Point out each malaria parasite and classify it by life-cycle stage.
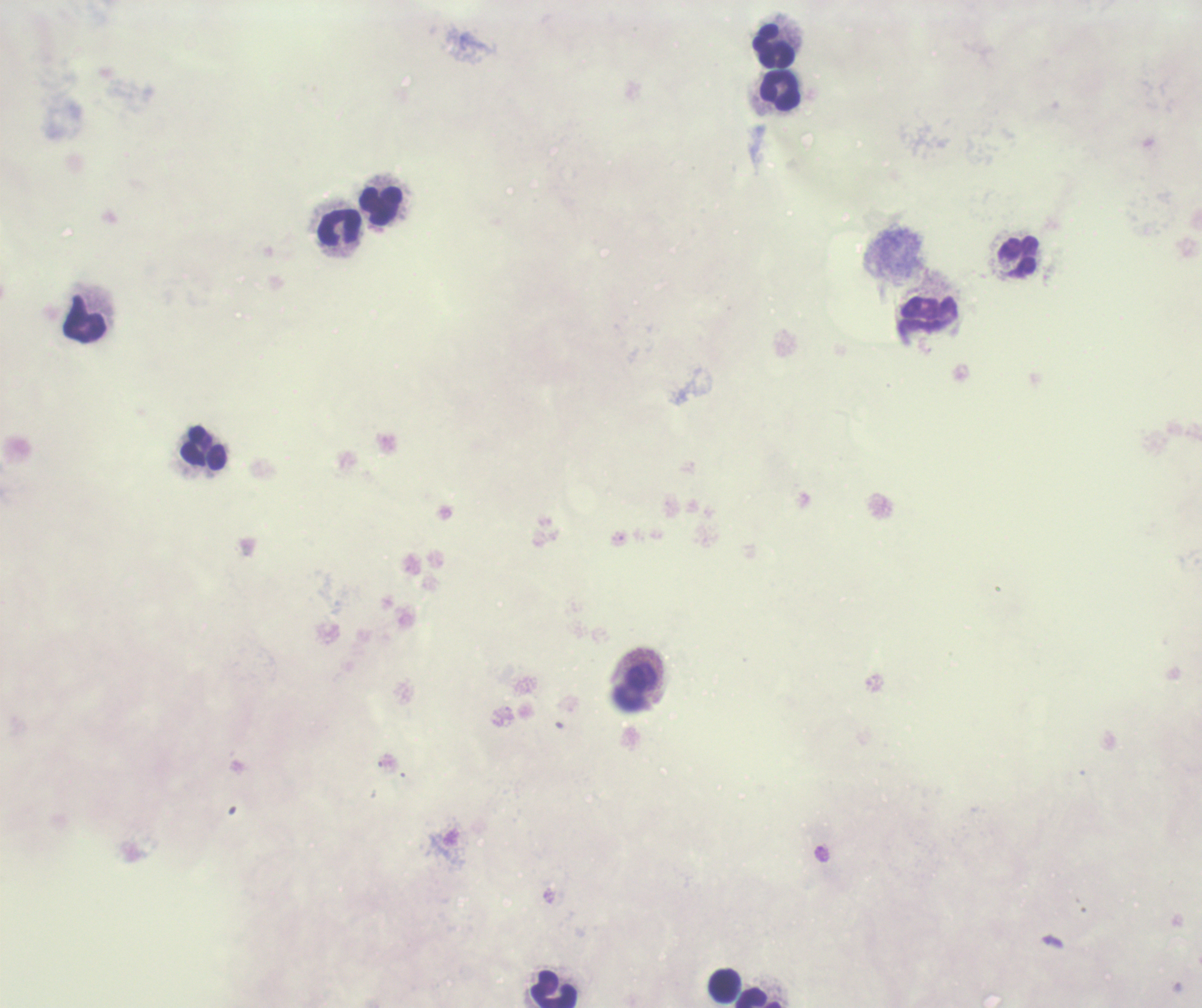
Negative for malaria parasites.

Approximate centers as {x, y} in pixels. Leukocyte locations: {773, 48}, {780, 91}, {381, 205}, {340, 228}, {1019, 256}, {85, 319}, {205, 448}, {636, 687}, {724, 985}, {554, 989}, {760, 998}. Captured at 100x magnification. Thick smear of blood. One field from this slide. Previously used in an actual diagnosis. Background quality: unsatisfactory. Coloration quality: bad. Romanowsky-stained preparation. Image is 1202×1008 pixels.